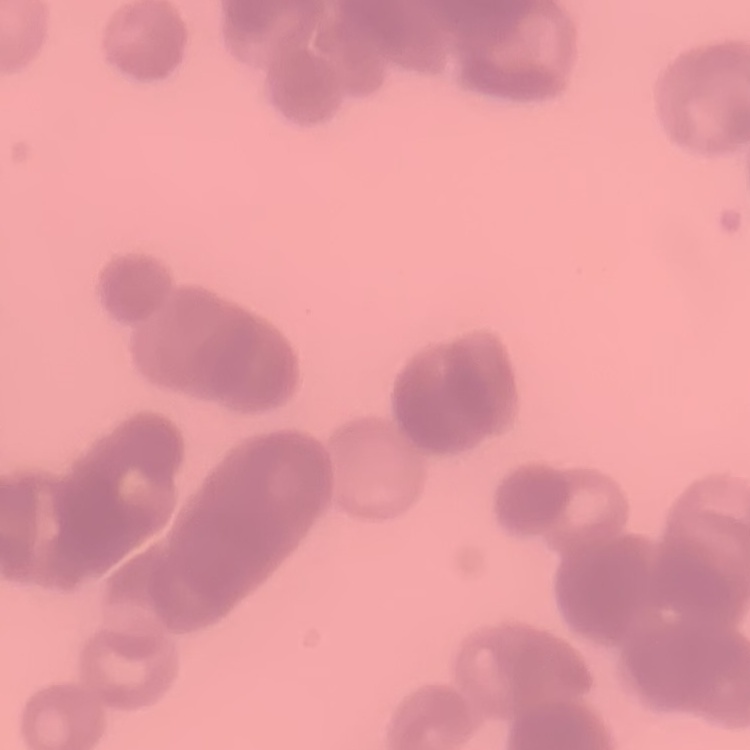

red blood cell morphology = rouleaux formation
preparation = thin blood smear
stain = Field's or Giemsa
image type = square crop of a larger photomicrograph